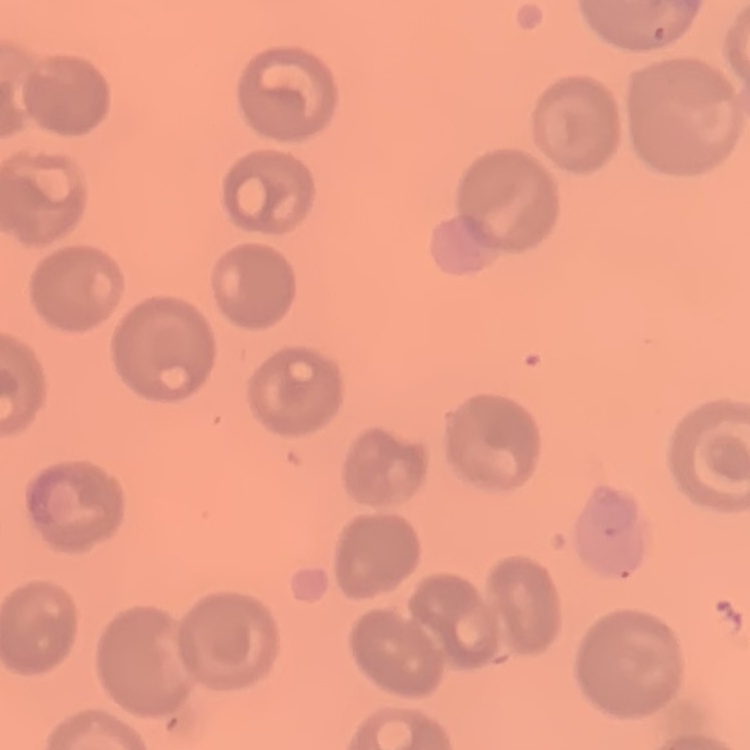
Summary:
  - Erythrocyte morphology: no rouleaux formation
  - Image type: one tile cut from a larger photomicrograph
  - Preparation: thin blood smear
  - Stain: Field's or Giemsa